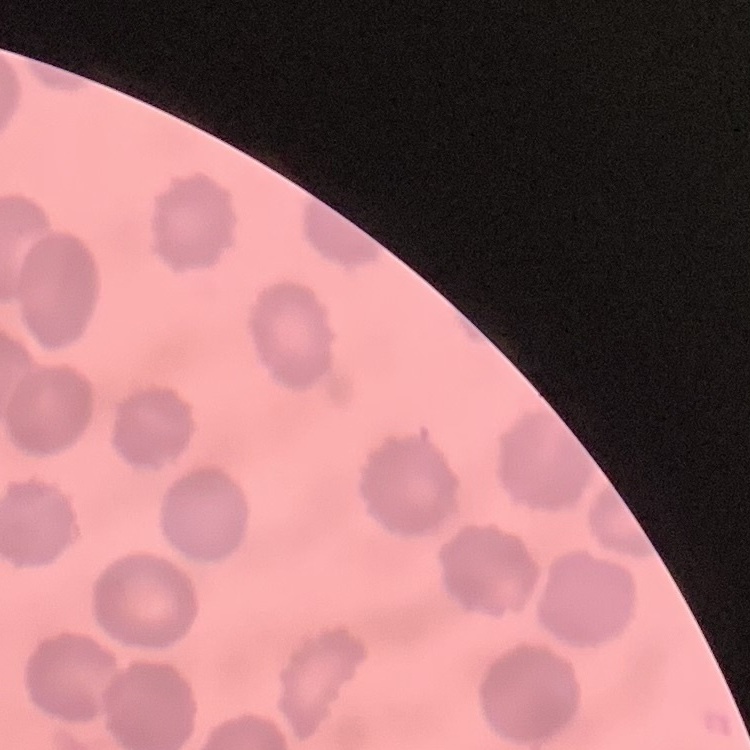
red blood cell morphology = no rouleaux formation
preparation = thin blood film
stain = Field's or Giemsa
image type = one tile cut from a larger photomicrograph